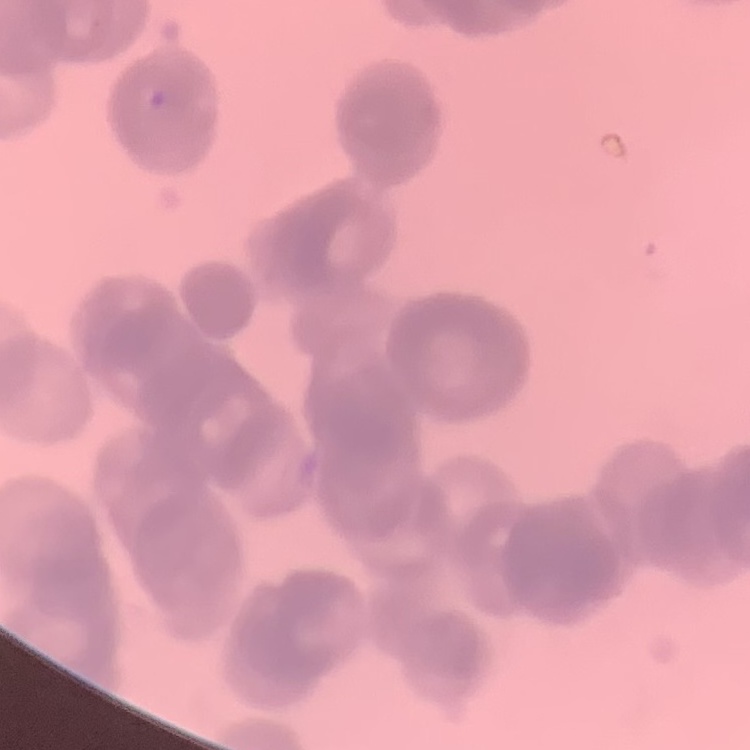
Summary:
  - Red blood cell morphology: rouleaux formation
  - Image type: one tile cut from a larger photomicrograph
  - Preparation: thin peripheral smear
  - Stain: Field's or Giemsa